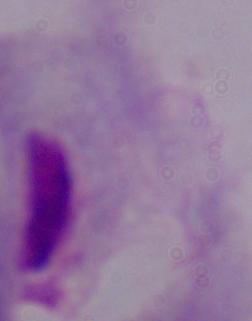

A trichomonad is seen. Micrograph. Captured at 1000x magnification.